Outline each blood parasite and name the species.
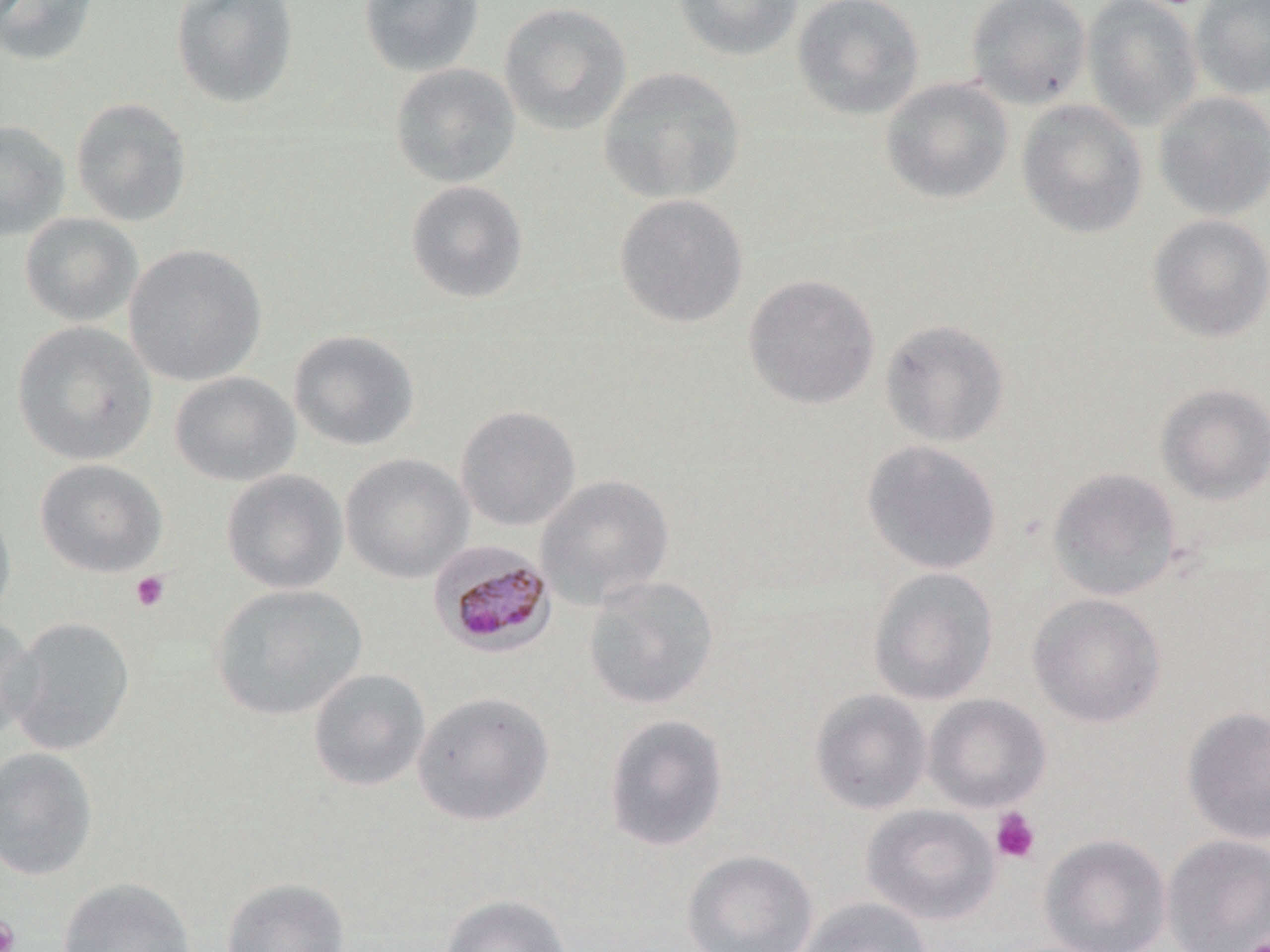
Approximate bounding boxes as named x1/y1/x2/y2 corners in pixels.
Plasmodium malariae-infected red blood cells: (x1=428, y1=539, x2=556, y2=657).
No Plasmodium falciparum, Plasmodium ovale, Plasmodium vivax, Babesia divergens, or Trypanosoma brucei observed.

{
  "slide_level_diagnosis": "Plasmodium malariae",
  "field_of_view": "one of a larger specimen",
  "platelet_locations": "approximate bounding boxes as named x1/y1/x2/y2 corners in pixels: (x1=130, y1=571, x2=170, y2=612), (x1=991, y1=807, x2=1040, y2=863), (x1=0, y1=916, x2=20, y2=952), (x1=1243, y1=933, x2=1269, y2=952)",
  "magnification": "1000x",
  "stain": "May-Grünwald-Giemsa",
  "uninfected_red_blood_cell_locations": "approximate bounding boxes as named x1/y1/x2/y2 corners in pixels: (x1=0, y1=0, x2=100, y2=67), (x1=171, y1=0, x2=300, y2=109), (x1=358, y1=0, x2=485, y2=77), (x1=673, y1=0, x2=804, y2=61), (x1=792, y1=0, x2=925, y2=121), (x1=965, y1=0, x2=1092, y2=110), (x1=1082, y1=0, x2=1203, y2=131), (x1=1190, y1=0, x2=1270, y2=100), (x1=498, y1=1, x2=632, y2=135), (x1=390, y1=63, x2=520, y2=187), (x1=598, y1=67, x2=746, y2=204), (x1=880, y1=77, x2=1013, y2=205), (x1=1153, y1=91, x2=1270, y2=221), (x1=71, y1=97, x2=192, y2=226), (x1=1016, y1=99, x2=1148, y2=239), (x1=0, y1=119, x2=70, y2=242), (x1=405, y1=179, x2=529, y2=304), (x1=614, y1=193, x2=749, y2=328), (x1=19, y1=212, x2=143, y2=327), (x1=1147, y1=213, x2=1270, y2=343), (x1=124, y1=243, x2=267, y2=386), (x1=743, y1=273, x2=880, y2=410), (x1=879, y1=318, x2=1011, y2=447), (x1=12, y1=321, x2=157, y2=465), (x1=288, y1=330, x2=419, y2=451), (x1=169, y1=371, x2=301, y2=487), (x1=1155, y1=383, x2=1270, y2=504), (x1=455, y1=405, x2=582, y2=531), (x1=861, y1=439, x2=1002, y2=575), (x1=340, y1=453, x2=474, y2=584), (x1=34, y1=459, x2=167, y2=577), (x1=1047, y1=467, x2=1183, y2=602), (x1=221, y1=468, x2=348, y2=594), (x1=535, y1=474, x2=674, y2=610), (x1=0, y1=495, x2=16, y2=626), (x1=867, y1=566, x2=999, y2=705), (x1=583, y1=575, x2=720, y2=710), (x1=210, y1=584, x2=368, y2=721), (x1=1027, y1=593, x2=1167, y2=728), (x1=0, y1=615, x2=41, y2=739), (x1=6, y1=616, x2=135, y2=756), (x1=307, y1=668, x2=431, y2=792), (x1=809, y1=688, x2=932, y2=815), (x1=411, y1=690, x2=555, y2=826), (x1=923, y1=693, x2=1051, y2=813), (x1=1181, y1=706, x2=1270, y2=845), (x1=603, y1=713, x2=729, y2=852), (x1=0, y1=746, x2=98, y2=881), (x1=861, y1=804, x2=1000, y2=925), (x1=1039, y1=833, x2=1172, y2=952), (x1=1161, y1=834, x2=1270, y2=952), (x1=682, y1=849, x2=819, y2=952), (x1=56, y1=877, x2=196, y2=952), (x1=221, y1=877, x2=350, y2=952), (x1=441, y1=893, x2=572, y2=952), (x1=797, y1=897, x2=933, y2=952)",
  "modality": "optical microscopy",
  "image_size": "1270×952 pixels",
  "preparation": "thin blood smear"
}